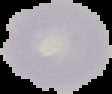

Summary:
  - Image type: segmented cell region with the area outside set to black
  - Preparation: thin blood smear
  - Image size: 112×94 pixels
  - Malaria status: uninfected